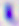

magnification = 400x
identification = Toxoplasma gondii
modality = photomicrograph